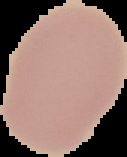

Malaria status: uninfected. Image is 127×157 pixels. From a thin blood film. Cell region segmented out of the field of view; the surrounding area is masked to black.